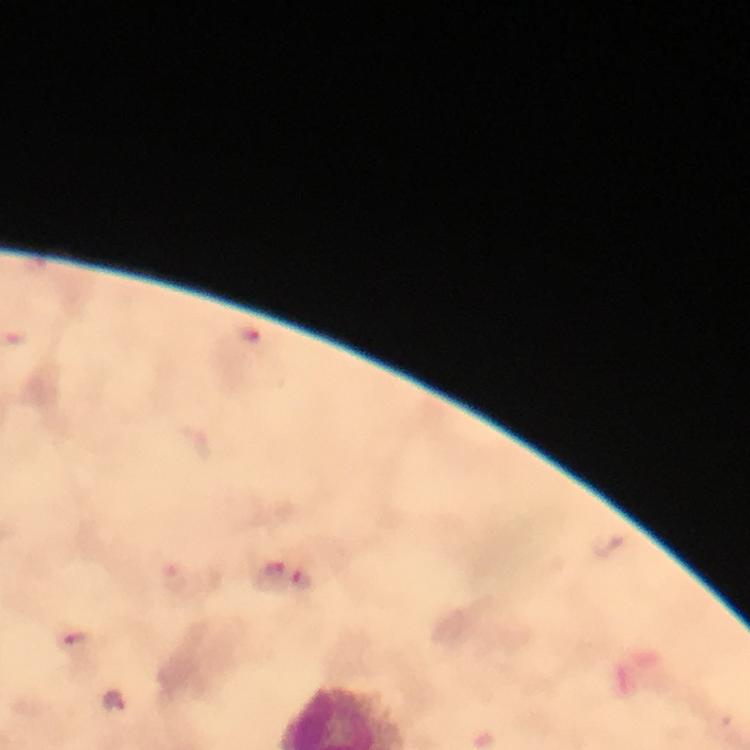
Approximate centers as [x, y] in pixels. Malaria parasite locations: [272, 570], [301, 578], [75, 636]. A crop from one field of view. Image is 750×750 pixels. Thick blood smear. Smartphone photograph taken through a microscope. Immersion oil applied. Giemsa-stained preparation. From a diagnostic examination for malaria. 100x magnification.